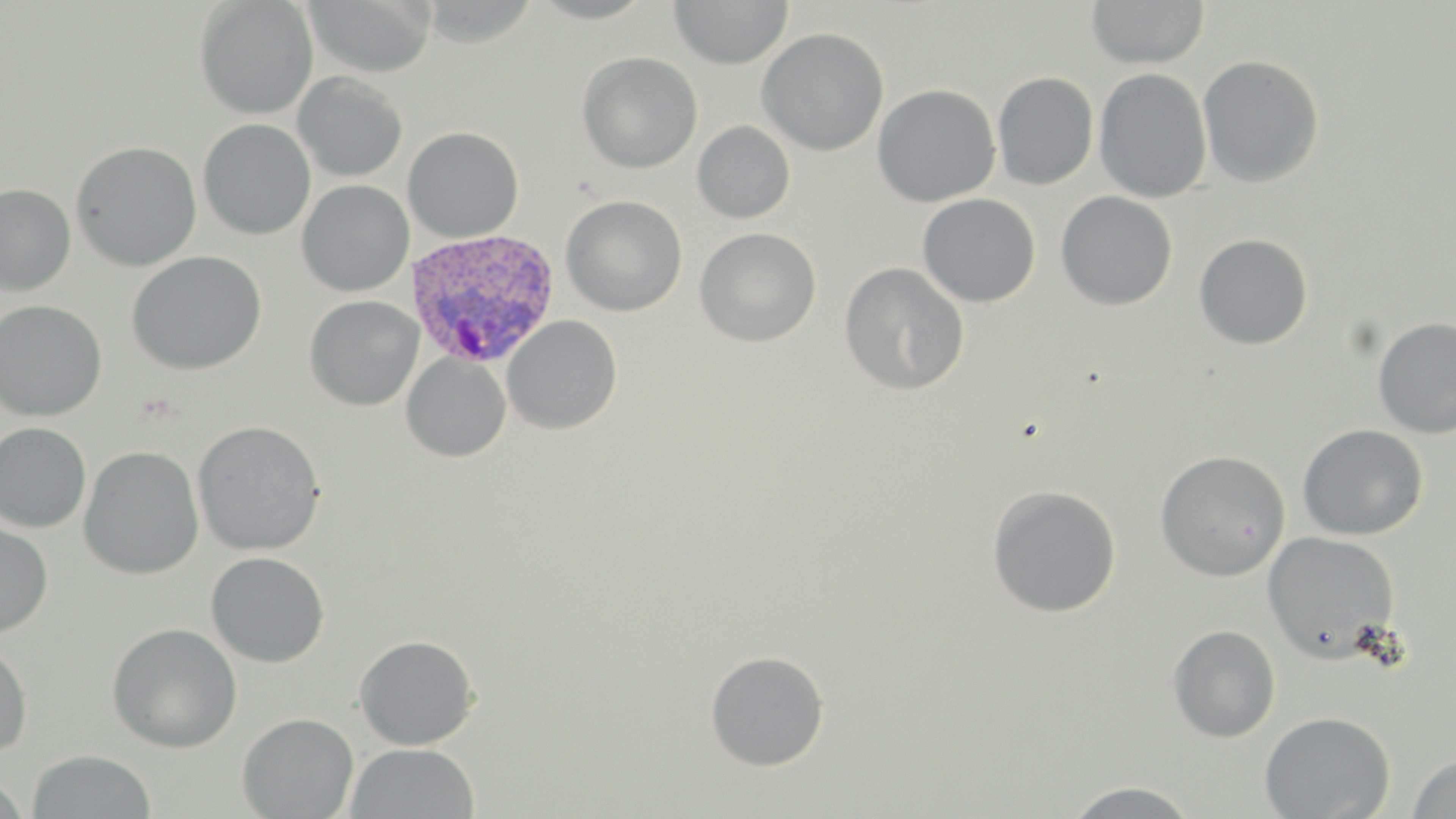
slide-level diagnosis = Plasmodium vivax
field of view = single
image size = 1456×819 pixels
uninfected red blood cell locations = approximate bounding boxes as named x1/y1/x2/y2 corners in pixels: (x1=194, y1=0, x2=319, y2=119), (x1=304, y1=0, x2=437, y2=77), (x1=668, y1=0, x2=793, y2=69), (x1=1086, y1=0, x2=1210, y2=69), (x1=756, y1=28, x2=889, y2=156), (x1=576, y1=52, x2=702, y2=173), (x1=1197, y1=54, x2=1324, y2=188), (x1=1094, y1=68, x2=1212, y2=203), (x1=293, y1=72, x2=408, y2=182), (x1=992, y1=72, x2=1099, y2=190), (x1=872, y1=84, x2=1001, y2=207), (x1=197, y1=119, x2=316, y2=240), (x1=692, y1=121, x2=795, y2=223), (x1=402, y1=126, x2=524, y2=243), (x1=71, y1=141, x2=202, y2=271), (x1=297, y1=179, x2=414, y2=297), (x1=0, y1=184, x2=75, y2=295), (x1=1055, y1=191, x2=1178, y2=311), (x1=917, y1=193, x2=1041, y2=307), (x1=561, y1=195, x2=688, y2=316), (x1=695, y1=227, x2=821, y2=347), (x1=1193, y1=233, x2=1313, y2=350), (x1=126, y1=251, x2=267, y2=375), (x1=839, y1=262, x2=969, y2=395), (x1=304, y1=295, x2=424, y2=411), (x1=0, y1=299, x2=107, y2=421), (x1=502, y1=314, x2=623, y2=435), (x1=1372, y1=316, x2=1456, y2=439), (x1=401, y1=352, x2=511, y2=462), (x1=191, y1=420, x2=326, y2=556), (x1=0, y1=423, x2=92, y2=533), (x1=1297, y1=424, x2=1428, y2=540), (x1=2, y1=426, x2=155, y2=562), (x1=79, y1=446, x2=204, y2=579), (x1=1154, y1=450, x2=1291, y2=581), (x1=986, y1=485, x2=1122, y2=618), (x1=0, y1=521, x2=53, y2=637), (x1=1261, y1=531, x2=1401, y2=661), (x1=205, y1=552, x2=330, y2=667), (x1=106, y1=622, x2=243, y2=752), (x1=1167, y1=624, x2=1281, y2=742), (x1=354, y1=634, x2=480, y2=750), (x1=0, y1=637, x2=33, y2=757), (x1=705, y1=650, x2=830, y2=771), (x1=1259, y1=711, x2=1395, y2=819), (x1=237, y1=712, x2=358, y2=818), (x1=347, y1=742, x2=480, y2=819), (x1=27, y1=750, x2=156, y2=818), (x1=1404, y1=753, x2=1456, y2=818), (x1=0, y1=774, x2=30, y2=818), (x1=1063, y1=781, x2=1201, y2=818)
stain = May-Grünwald-Giemsa
Plasmodium vivax-infected red blood cell locations = approximate bounding boxes as named x1/y1/x2/y2 corners in pixels: (x1=406, y1=228, x2=561, y2=369)
preparation = thin blood film
modality = optical microscopy
magnification = 1000x